Evaluate for malaria.
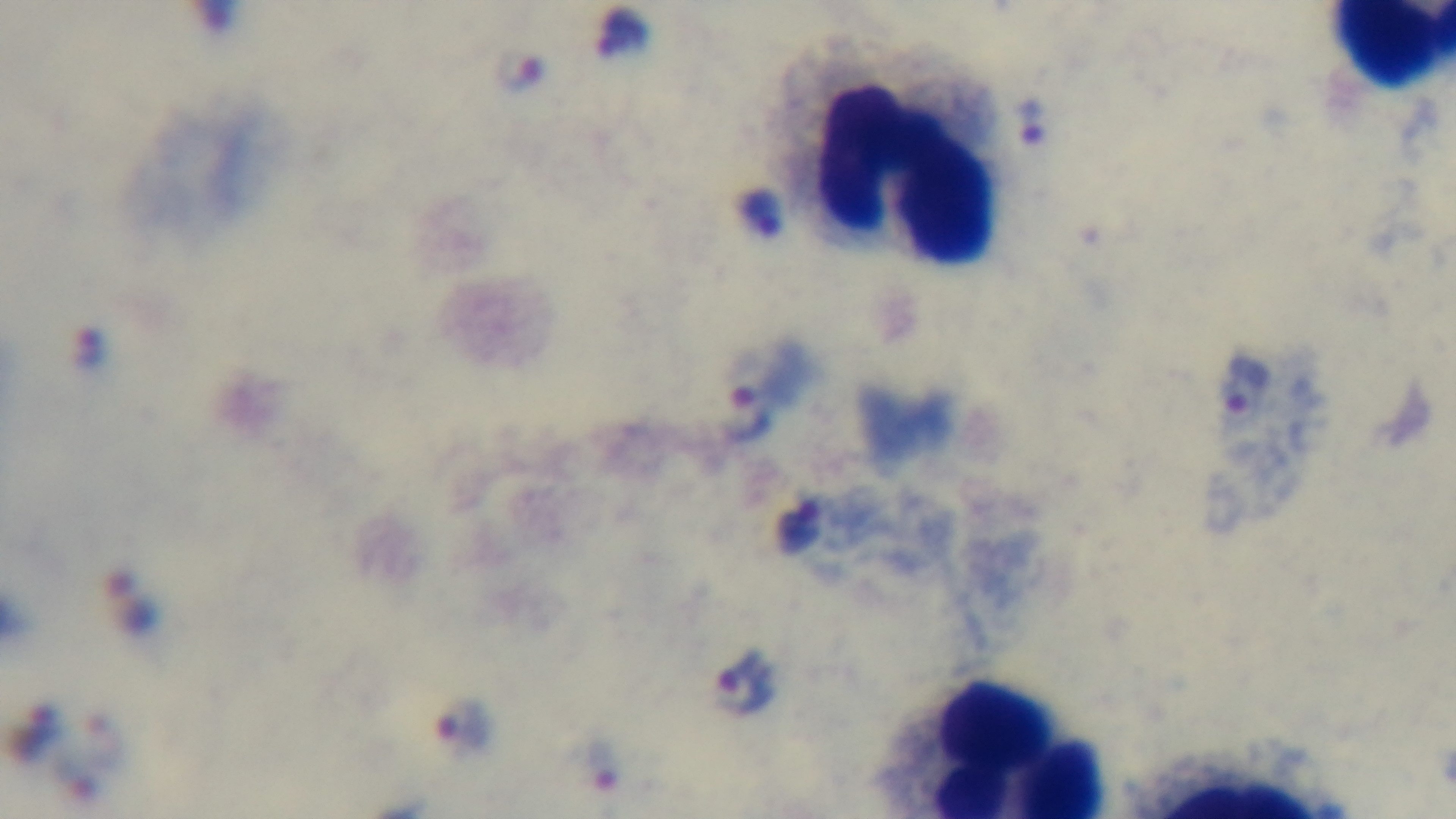

It is infected.

Giemsa-stained. Preparation: thick smear. Oil-immersion objective, 100x. Photomicrograph. Single field of view. Mounted 4K digital camera.